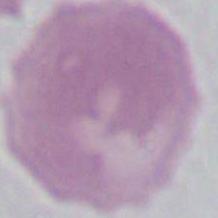

identification = erythrocyte
magnification = 1000x
modality = micrograph